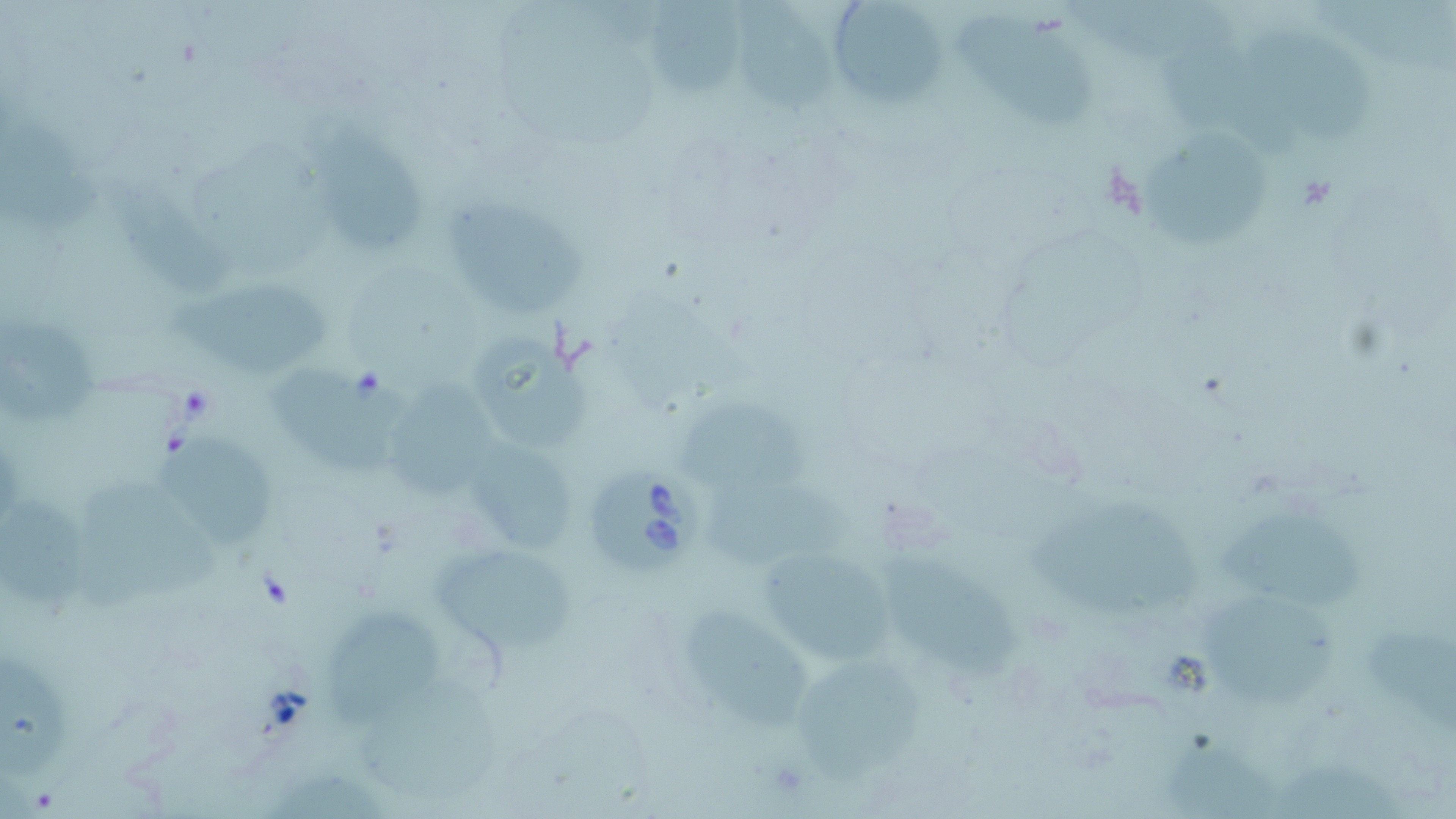

Summary:
  - Coordinate format: approximate bounding boxes as [x1, y1, x2, y2] in pixels
  - Babesia divergens-infected red blood cell locations: [584, 469, 705, 580]
  - Uninfected red blood cell locations: [650, 0, 746, 97], [738, 0, 839, 110], [1060, 0, 1248, 63], [827, 2, 948, 107], [956, 12, 1104, 128], [1252, 32, 1381, 141], [1162, 42, 1301, 156], [0, 113, 103, 234], [1137, 123, 1268, 251], [302, 125, 429, 252], [108, 171, 238, 296], [442, 196, 593, 320], [169, 285, 330, 377], [0, 315, 97, 433], [469, 332, 594, 454], [267, 360, 411, 474], [384, 369, 504, 494], [678, 398, 817, 497], [156, 440, 275, 543], [464, 441, 585, 551], [78, 471, 226, 618], [703, 476, 857, 568], [1, 497, 95, 605], [1031, 498, 1197, 621], [1216, 505, 1363, 611], [433, 540, 575, 654], [757, 543, 894, 667], [877, 545, 1024, 687], [1196, 591, 1344, 701], [687, 600, 817, 726], [320, 609, 438, 721], [1369, 623, 1456, 735], [0, 653, 67, 782], [790, 658, 926, 785], [356, 681, 501, 801], [1159, 740, 1296, 817], [1278, 754, 1412, 818]
  - Slide-level diagnosis: Babesia divergens
  - Modality: light microscopy
  - Preparation: thin blood film
  - Magnification: 1000x
  - Stain: May-Grünwald-Giemsa
  - Field of view: single
  - Image size: 1456×819 pixels